Name the blood parasite species.
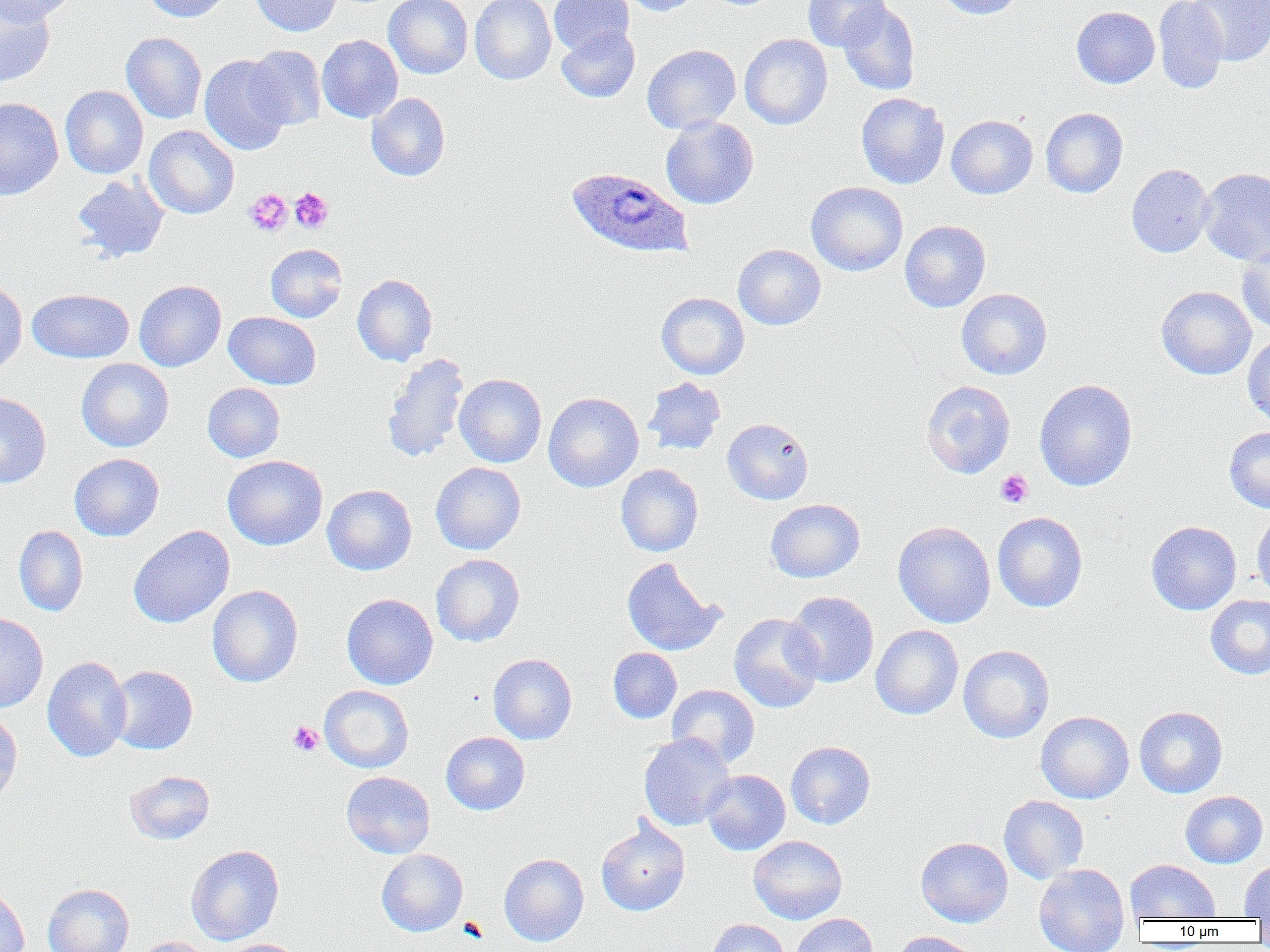

Plasmodium ovale.

magnification: 1000x
modality: optical microscopy
preparation: thin blood smear
image_size: 1270×952 pixels
field_of_view: single
plasmodium_ovale_infected_red_blood_cell_locations: 'approximate bounding boxes as (x1, y1, x2, y2) in pixels: (565, 167, 692, 259)'
platelet_locations: 'approximate bounding boxes as (x1, y1, x2, y2) in pixels: (288, 187, 333, 234), (244, 189, 292, 236), (995, 469, 1033, 508), (287, 720, 323, 756)'
uninfected_red_blood_cell_locations: 'approximate bounding boxes as (x1, y1, x2, y2) in pixels: (0, 0, 55, 87), (0, 0, 76, 25), (142, 0, 233, 22), (250, 0, 342, 36), (384, 0, 473, 79), (469, 0, 556, 84), (548, 0, 634, 57), (620, 0, 702, 16), (803, 0, 890, 51), (935, 0, 1023, 19), (1154, 1, 1229, 93), (1188, 1, 1270, 65), (838, 3, 921, 96), (1071, 6, 1160, 88), (556, 27, 640, 102), (121, 32, 207, 124), (739, 34, 833, 129), (316, 35, 403, 123), (245, 44, 326, 130), (642, 44, 741, 133), (199, 55, 293, 155), (60, 85, 149, 179), (856, 92, 949, 189), (366, 93, 450, 181), (0, 97, 64, 200), (1040, 107, 1128, 198), (660, 115, 758, 209), (946, 115, 1037, 199), (143, 125, 239, 219), (1126, 164, 1214, 257), (1198, 168, 1270, 265), (72, 175, 169, 263), (806, 181, 908, 276), (899, 220, 991, 312), (265, 243, 347, 322), (1237, 243, 1270, 335), (733, 245, 825, 330), (352, 274, 437, 366), (0, 278, 27, 376), (134, 280, 227, 371), (1156, 286, 1257, 380), (27, 288, 134, 363), (956, 288, 1052, 379), (656, 292, 749, 379), (224, 312, 321, 389), (1242, 334, 1270, 428), (382, 352, 470, 464), (76, 358, 174, 452), (454, 374, 547, 467), (642, 376, 727, 456), (1034, 379, 1137, 491), (921, 380, 1015, 478), (202, 383, 285, 463), (453, 383, 644, 475), (0, 391, 51, 489), (543, 392, 644, 492), (722, 418, 813, 505), (1224, 426, 1270, 512), (69, 453, 164, 541), (222, 455, 328, 550), (430, 462, 526, 555), (616, 464, 703, 557), (322, 484, 417, 575), (765, 499, 865, 583), (1251, 510, 1270, 600), (992, 511, 1088, 612), (893, 521, 995, 628), (1146, 521, 1242, 615), (14, 525, 88, 616), (128, 525, 235, 628), (431, 553, 525, 646), (621, 557, 724, 656), (207, 585, 303, 687), (784, 591, 879, 687), (341, 593, 438, 689), (1205, 595, 1270, 679), (0, 612, 48, 713), (728, 613, 824, 713), (871, 625, 964, 719), (958, 645, 1055, 743), (608, 647, 682, 723), (488, 653, 577, 744), (42, 656, 132, 762), (108, 665, 198, 754), (667, 684, 760, 767), (319, 685, 414, 773), (1134, 706, 1228, 798), (0, 708, 23, 810), (1036, 711, 1135, 804), (441, 732, 530, 815), (638, 732, 735, 831), (785, 741, 875, 829), (702, 769, 790, 855), (124, 770, 215, 845), (341, 771, 436, 859), (1180, 791, 1268, 868), (998, 795, 1089, 883), (595, 818, 691, 916), (748, 835, 847, 924), (916, 837, 1013, 927), (186, 844, 284, 945), (376, 849, 468, 936), (499, 853, 589, 946), (1125, 859, 1220, 923), (1239, 860, 1270, 920), (1033, 864, 1129, 952), (43, 883, 134, 952), (0, 885, 30, 952), (789, 913, 879, 952), (704, 919, 791, 952), (891, 931, 980, 952), (133, 937, 214, 952), (217, 939, 309, 952)'